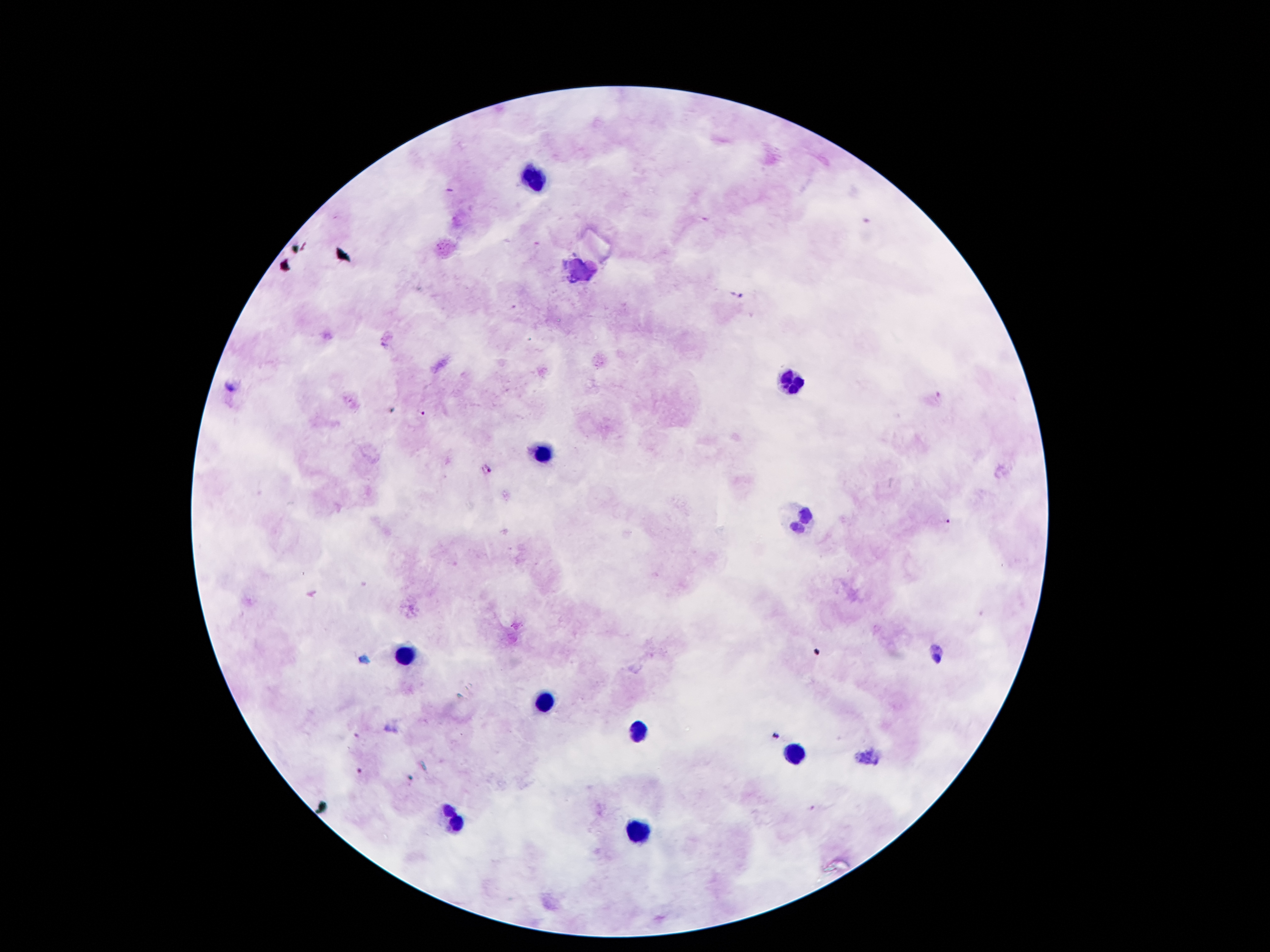
coordinate format = approximate object centers, in pixels from the top-left corner
leukocyte locations = (x=535, y=178), (x=583, y=273), (x=792, y=382), (x=540, y=455), (x=799, y=517), (x=404, y=658), (x=544, y=705), (x=640, y=733), (x=794, y=751), (x=449, y=825), (x=640, y=834)
malaria parasite locations = (x=737, y=295), (x=382, y=345), (x=231, y=386), (x=421, y=413), (x=485, y=469), (x=945, y=522), (x=868, y=756)
capture = smartphone through the microscope eyepiece
stain = Giemsa
patient malaria status = infected with Plasmodium falciparum
image size = 1270×952 pixels
field of view = single
preparation = thick blood film
magnification = 100x